Identify the parasite.
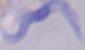

This is a trypanosome.

{
  "modality": "micrograph",
  "magnification": "1000x"
}